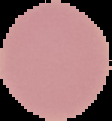

Result: no Plasmodium parasites seen. Cell region segmented out of the field of view; the surrounding area is masked to black. From a thin blood smear. Image is 112×121 pixels.